Locate and identify every blood parasite.
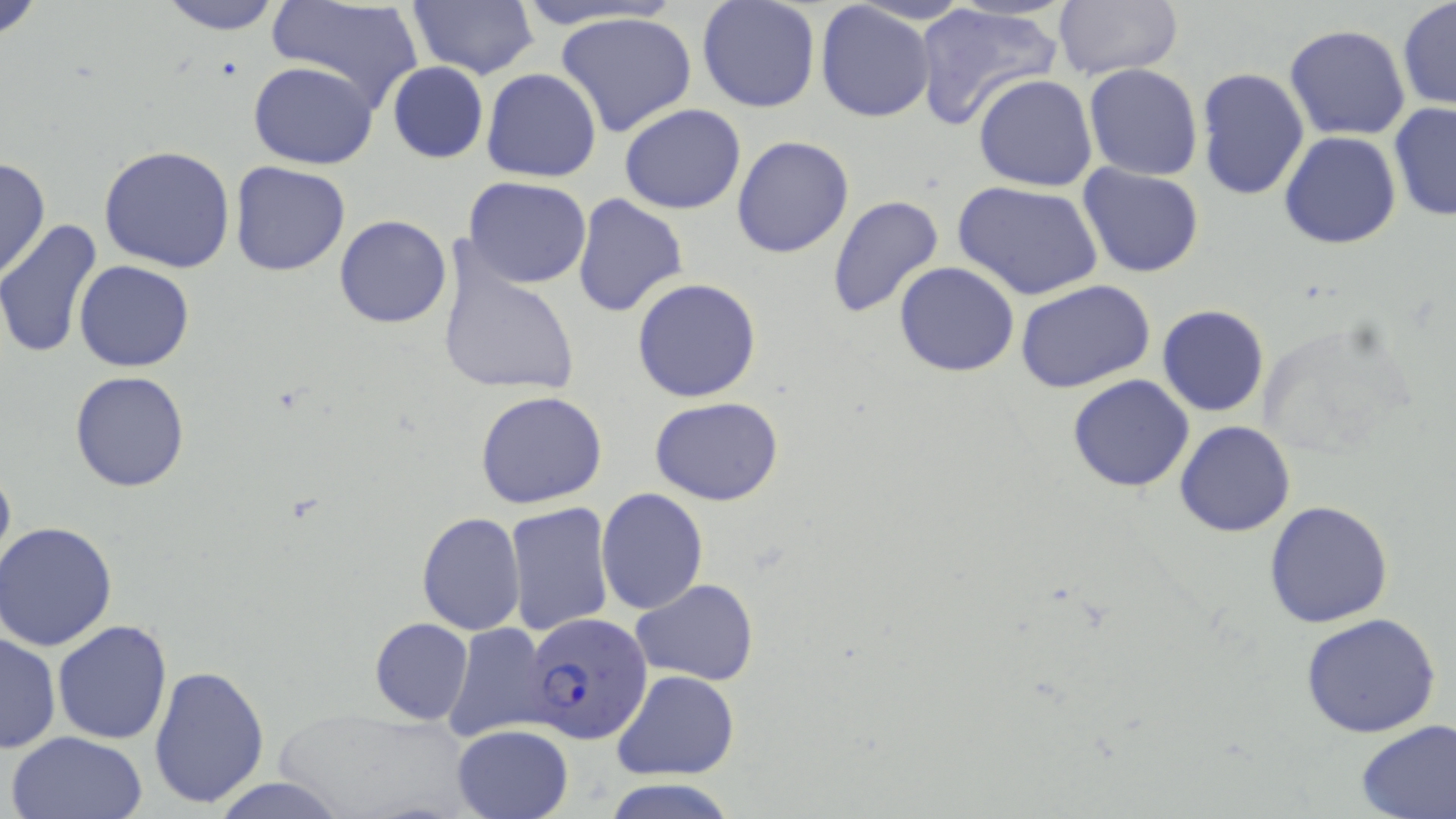
Approximate bounding boxes as [x1, y1, x2, y2] in pixels.
Plasmodium falciparum-infected red blood cells: [526, 613, 654, 742].
No Plasmodium ovale, Plasmodium malariae, Plasmodium vivax, Babesia divergens, or Trypanosoma brucei observed.

Summary:
  - Uninfected red blood cell locations: [0, 0, 48, 43], [153, 0, 288, 35], [265, 0, 425, 112], [406, 0, 538, 81], [509, 0, 683, 31], [1051, 0, 1185, 80], [696, 1, 821, 114], [912, 2, 1060, 131], [1397, 2, 1455, 111], [815, 3, 935, 124], [554, 10, 700, 140], [1283, 23, 1412, 140], [248, 61, 379, 168], [387, 62, 489, 164], [1083, 64, 1204, 181], [1195, 67, 1310, 201], [481, 68, 602, 183], [972, 74, 1098, 192], [1388, 103, 1456, 222], [620, 104, 746, 215], [1279, 131, 1402, 249], [732, 136, 854, 258], [99, 144, 236, 273], [0, 157, 49, 281], [228, 162, 350, 277], [1078, 164, 1204, 277], [465, 176, 592, 288], [953, 179, 1102, 302], [572, 194, 687, 318], [827, 194, 945, 320], [334, 214, 453, 328], [0, 220, 104, 361], [438, 252, 583, 398], [74, 260, 194, 372], [894, 262, 1020, 377], [631, 278, 762, 403], [1015, 279, 1156, 393], [1157, 304, 1270, 417], [69, 371, 192, 492], [1067, 374, 1195, 492], [476, 390, 609, 510], [650, 395, 784, 505], [1173, 421, 1295, 538], [0, 461, 15, 579], [597, 487, 708, 615], [1264, 499, 1395, 629], [505, 502, 614, 637], [417, 512, 525, 636], [1, 523, 120, 650], [631, 578, 759, 686], [1300, 612, 1441, 738], [368, 617, 473, 724], [52, 619, 173, 745], [442, 622, 553, 743], [0, 631, 61, 753], [148, 664, 272, 807], [612, 669, 738, 779], [1355, 719, 1456, 819], [451, 725, 575, 819], [6, 730, 149, 819], [210, 778, 350, 817], [600, 780, 738, 818]
  - Slide-level diagnosis: Plasmodium falciparum
  - Magnification: 1000x
  - Preparation: thin blood film
  - Field of view: one of a larger specimen
  - Modality: light microscopy
  - Image size: 1456×819 pixels
  - Stain: May-Grünwald-Giemsa